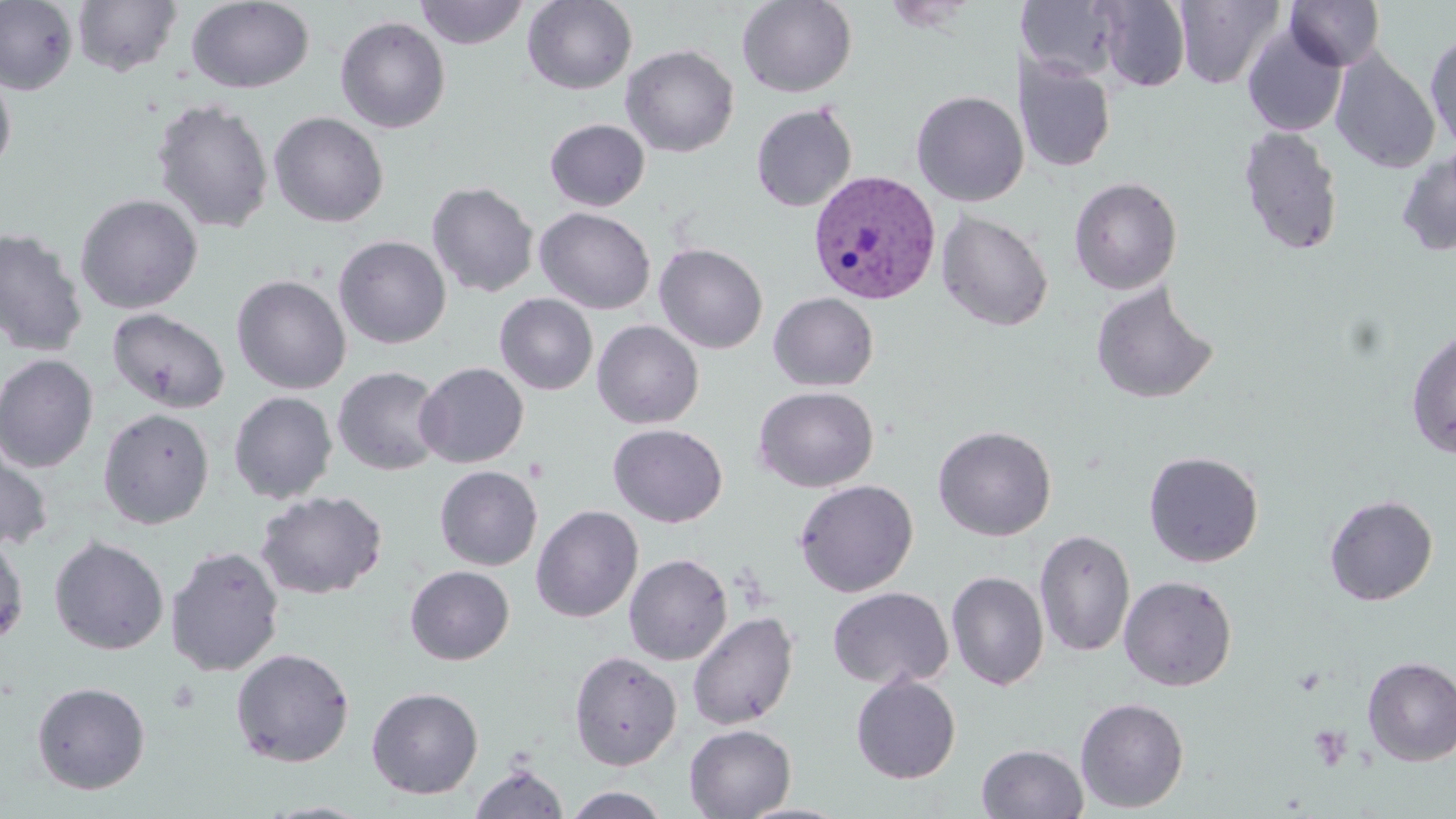
Approximate bounding boxes as named x1/y1/x2/y2 corners in pixels. Plasmodium vivax-infected red blood cell locations: (x1=808, y1=170, x2=942, y2=305). Uninfected red blood cell locations: (x1=0, y1=0, x2=79, y2=95), (x1=414, y1=0, x2=529, y2=49), (x1=522, y1=0, x2=637, y2=94), (x1=737, y1=0, x2=857, y2=98), (x1=1093, y1=0, x2=1192, y2=92), (x1=1174, y1=0, x2=1286, y2=89), (x1=1285, y1=0, x2=1385, y2=71), (x1=72, y1=1, x2=182, y2=76), (x1=186, y1=1, x2=314, y2=93), (x1=1019, y1=2, x2=1123, y2=83), (x1=335, y1=16, x2=451, y2=134), (x1=1241, y1=23, x2=1347, y2=137), (x1=1425, y1=30, x2=1456, y2=153), (x1=621, y1=45, x2=739, y2=157), (x1=1330, y1=50, x2=1440, y2=173), (x1=1017, y1=56, x2=1115, y2=173), (x1=0, y1=68, x2=17, y2=176), (x1=911, y1=90, x2=1029, y2=206), (x1=151, y1=98, x2=274, y2=234), (x1=751, y1=102, x2=858, y2=212), (x1=269, y1=111, x2=389, y2=228), (x1=544, y1=119, x2=650, y2=211), (x1=1238, y1=125, x2=1344, y2=256), (x1=1396, y1=148, x2=1456, y2=257), (x1=1068, y1=177, x2=1182, y2=295), (x1=427, y1=182, x2=540, y2=297), (x1=75, y1=193, x2=204, y2=314), (x1=534, y1=207, x2=656, y2=314), (x1=936, y1=209, x2=1053, y2=332), (x1=0, y1=227, x2=89, y2=358), (x1=333, y1=235, x2=452, y2=349), (x1=654, y1=242, x2=768, y2=354), (x1=231, y1=274, x2=351, y2=395), (x1=1090, y1=280, x2=1219, y2=405), (x1=768, y1=292, x2=879, y2=391), (x1=494, y1=293, x2=598, y2=396), (x1=107, y1=307, x2=231, y2=414), (x1=592, y1=320, x2=704, y2=429), (x1=1405, y1=327, x2=1456, y2=459), (x1=0, y1=353, x2=99, y2=473), (x1=414, y1=362, x2=529, y2=468), (x1=331, y1=366, x2=446, y2=476), (x1=753, y1=386, x2=879, y2=492), (x1=228, y1=391, x2=337, y2=504), (x1=98, y1=408, x2=214, y2=529), (x1=608, y1=424, x2=727, y2=528), (x1=933, y1=425, x2=1056, y2=541), (x1=0, y1=438, x2=54, y2=554), (x1=1143, y1=450, x2=1264, y2=568), (x1=435, y1=465, x2=543, y2=570), (x1=793, y1=479, x2=919, y2=597), (x1=255, y1=490, x2=388, y2=600), (x1=1323, y1=494, x2=1438, y2=606), (x1=531, y1=505, x2=643, y2=622), (x1=1034, y1=528, x2=1135, y2=659), (x1=0, y1=531, x2=29, y2=648), (x1=48, y1=536, x2=169, y2=655), (x1=165, y1=545, x2=285, y2=677), (x1=624, y1=553, x2=732, y2=665), (x1=405, y1=565, x2=515, y2=665), (x1=946, y1=571, x2=1049, y2=690), (x1=1119, y1=575, x2=1238, y2=691), (x1=827, y1=587, x2=953, y2=690), (x1=688, y1=611, x2=799, y2=730), (x1=230, y1=647, x2=355, y2=767), (x1=568, y1=650, x2=682, y2=770), (x1=1361, y1=656, x2=1456, y2=766), (x1=850, y1=675, x2=961, y2=784), (x1=31, y1=681, x2=151, y2=794), (x1=366, y1=686, x2=484, y2=799), (x1=1075, y1=697, x2=1189, y2=813), (x1=684, y1=724, x2=795, y2=819), (x1=977, y1=743, x2=1089, y2=819), (x1=469, y1=762, x2=569, y2=819), (x1=563, y1=786, x2=669, y2=818), (x1=258, y1=800, x2=379, y2=818), (x1=736, y1=802, x2=855, y2=819). Platelet locations: (x1=1308, y1=724, x2=1353, y2=771). Slide-level diagnosis: Plasmodium vivax. Captured at 1000x magnification. One field of a larger specimen. Image is 1456×819 pixels. Light microscopy. May-Grünwald-Giemsa-stained preparation. Thin blood film.